Give the extent of all Plasmodium falciparum-infected red blood cells.
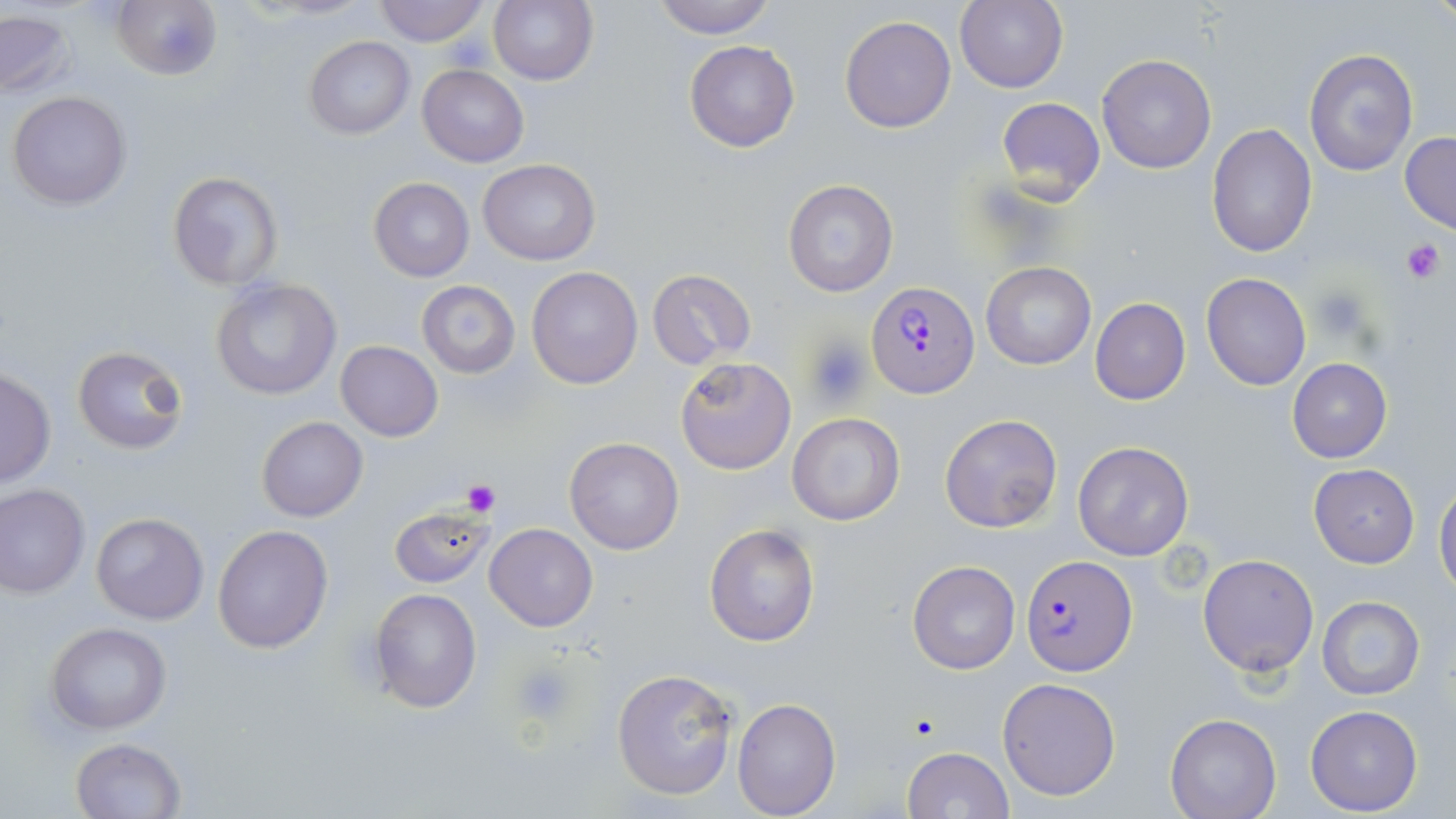
Approximate bounding boxes as [x1, y1, x2, y2] in pixels.
Plasmodium falciparum-infected red blood cells: [866, 282, 980, 399], [1022, 555, 1137, 676].

slide-level diagnosis = Plasmodium falciparum
uninfected red blood cell locations = approximate bounding boxes as [x1, y1, x2, y2] in pixels: [112, 0, 223, 80], [372, 0, 492, 46], [489, 0, 597, 86], [650, 0, 778, 38], [955, 0, 1070, 94], [0, 9, 77, 100], [839, 15, 957, 134], [303, 35, 415, 140], [684, 40, 799, 152], [1303, 48, 1418, 178], [1097, 55, 1216, 173], [417, 64, 529, 166], [7, 91, 131, 211], [995, 97, 1106, 205], [1207, 122, 1317, 259], [1399, 132, 1456, 234], [479, 159, 601, 265], [167, 170, 283, 290], [368, 177, 474, 281], [782, 178, 899, 299], [981, 261, 1096, 369], [527, 266, 643, 389], [647, 269, 756, 369], [1202, 273, 1311, 391], [211, 277, 342, 400], [416, 280, 521, 378], [1090, 298, 1190, 405], [335, 340, 441, 442], [72, 346, 191, 456], [674, 356, 796, 474], [1287, 357, 1393, 463], [1, 367, 56, 487], [787, 413, 905, 526], [939, 414, 1063, 534], [256, 416, 368, 522], [563, 437, 684, 556], [1073, 441, 1194, 561], [1308, 465, 1420, 568], [1434, 479, 1456, 596], [0, 485, 90, 598], [389, 504, 495, 589], [90, 512, 209, 625], [703, 523, 820, 648], [485, 524, 599, 631], [212, 526, 332, 653], [1197, 553, 1320, 678], [907, 560, 1021, 675], [369, 588, 482, 713], [1316, 596, 1426, 700], [46, 622, 171, 735], [612, 669, 738, 801], [997, 676, 1121, 802], [731, 696, 841, 819], [1305, 705, 1424, 816], [1165, 714, 1283, 819], [72, 738, 186, 819], [901, 746, 1014, 819]
preparation = thin blood film
magnification = 1000x
stain = May-Grünwald-Giemsa
modality = optical microscopy
platelet locations = approximate bounding boxes as [x1, y1, x2, y2] in pixels: [446, 32, 495, 70], [1401, 237, 1446, 284], [1307, 286, 1370, 341], [807, 335, 871, 407], [461, 479, 498, 516], [514, 661, 576, 723]
field of view = single
image size = 1456×819 pixels